Report the malaria status of this cell.
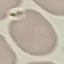

Uninfected.

Thin blood smear. Acquired by smartphone through the microscope eyepiece. Giemsa stain. Automatically extracted cell patch, resized to 64 × 64 pixels.